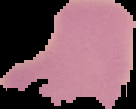

preparation = thin blood smear
image type = segmented cell region on a black background
image size = 136×109 pixels
result = negative for Plasmodium parasites